Comment on the morphology of the erythrocytes.
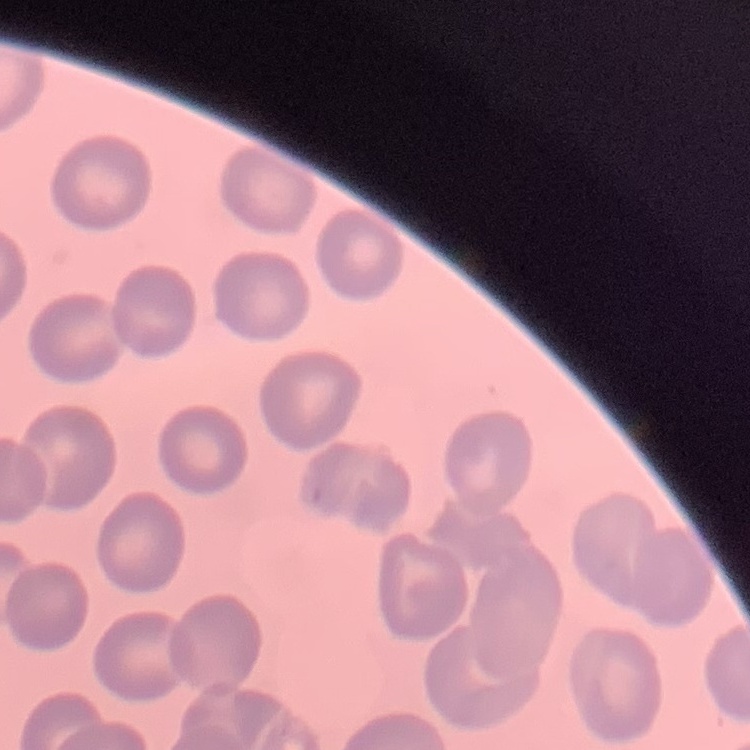
They show no rouleaux formation.

preparation = thin blood film
image type = one tile cut from a larger photomicrograph
stain = Field's or Giemsa